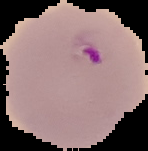
Summary:
  - Preparation: thin blood smear
  - Image size: 148×151 pixels
  - Image type: segmented cell region on a black background
  - Result: malaria parasites detected